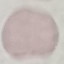

Malaria status: uninfected. Giemsa stain. Thin smear of blood. Acquired by smartphone through the microscope eyepiece. Automatically extracted cell patch, resized to 64 × 64 pixels.